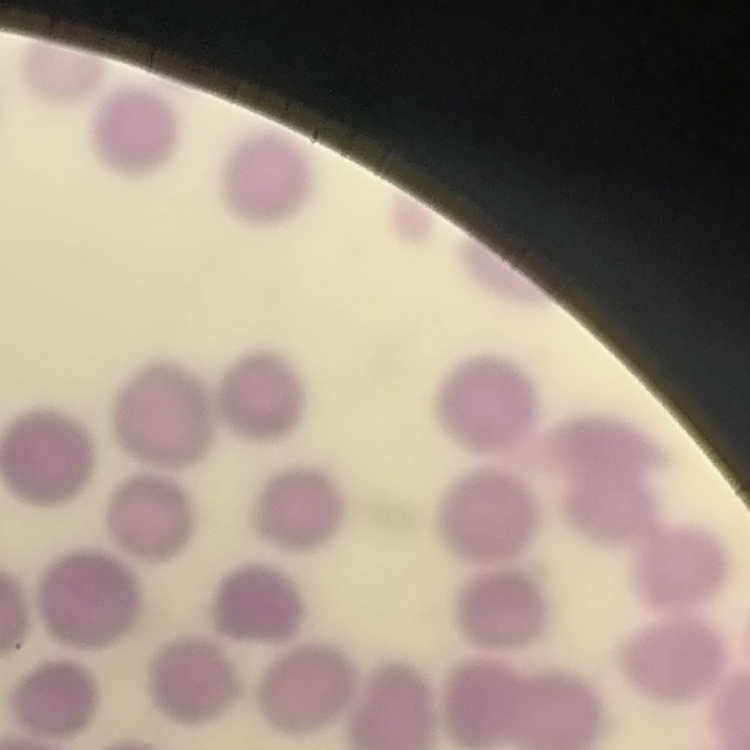

Summary:
  - Red blood cell morphology: no rouleaux formation
  - Preparation: thin peripheral smear
  - Stain: Field's or Giemsa
  - Image type: one tile cut from a larger photomicrograph